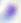
Micrograph. 400x magnification. Toxoplasma gondii is seen.